State which parasite is depicted.
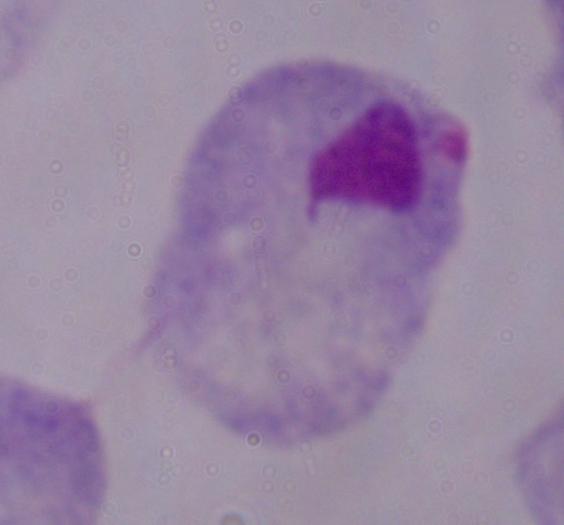

A trichomonad.

magnification = 1000x
modality = micrograph